Evaluate for parasitized red blood cells.
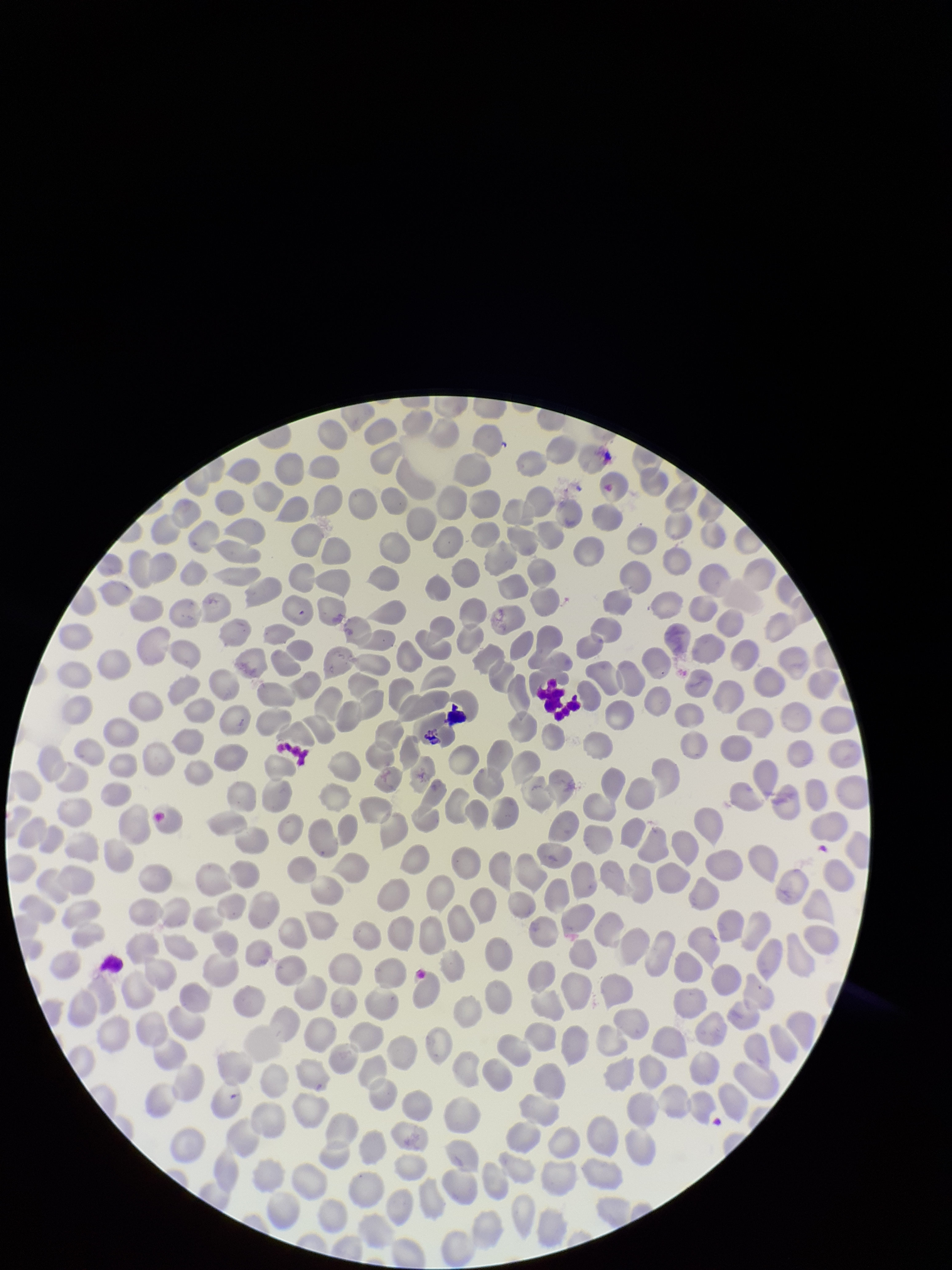

None detected.

Summary:
  - Image size: 952×1270 pixels
  - Capture: smartphone photograph through the microscope eyepiece
  - Preparation: thin blood smear
  - Patient malaria status: negative
  - Red blood cell count: 342
  - Field of view: one from this slide
  - Parasitized red blood cell count: 0
  - Stain: Giemsa